Comment on the morphology of the red blood cells.
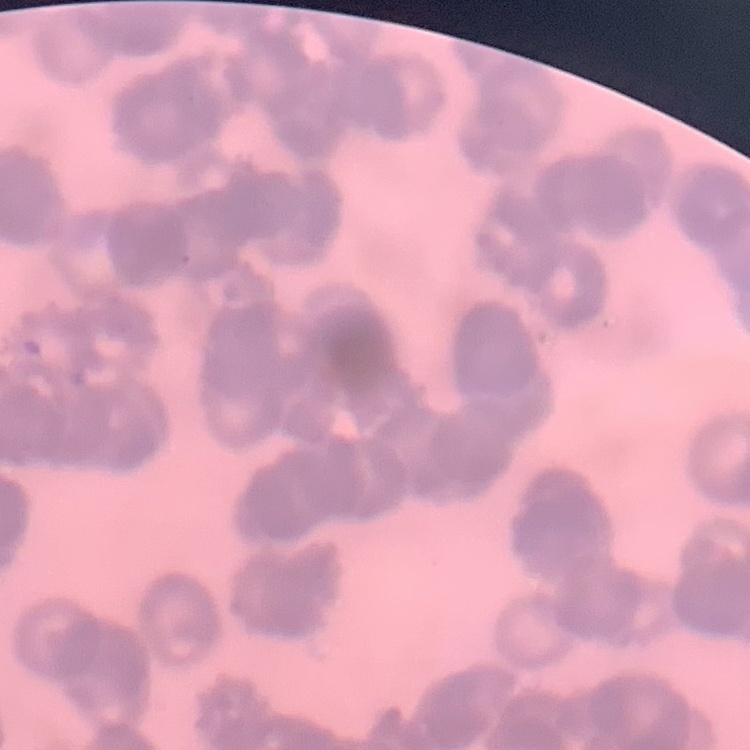

They show rouleaux formation.

Square crop of a larger photomicrograph. Thin blood film. Field's or Giemsa stain.